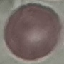
Summary:
  - Result: no malaria parasites detected
  - Capture: smartphone through the microscope eyepiece
  - Stain: Giemsa
  - Image type: automatically extracted cell patch, resized to 64 × 64 pixels
  - Preparation: thin blood film